Identify the cell.
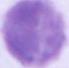

This is an erythrocyte.

{
  "modality": "photomicrograph",
  "magnification": "1000x"
}